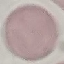

result: no malaria parasites seen
preparation: thin blood smear
image_type: automatically extracted cell patch, resized to 64 × 64 pixels
capture: smartphone camera at the microscope eyepiece
stain: Giemsa